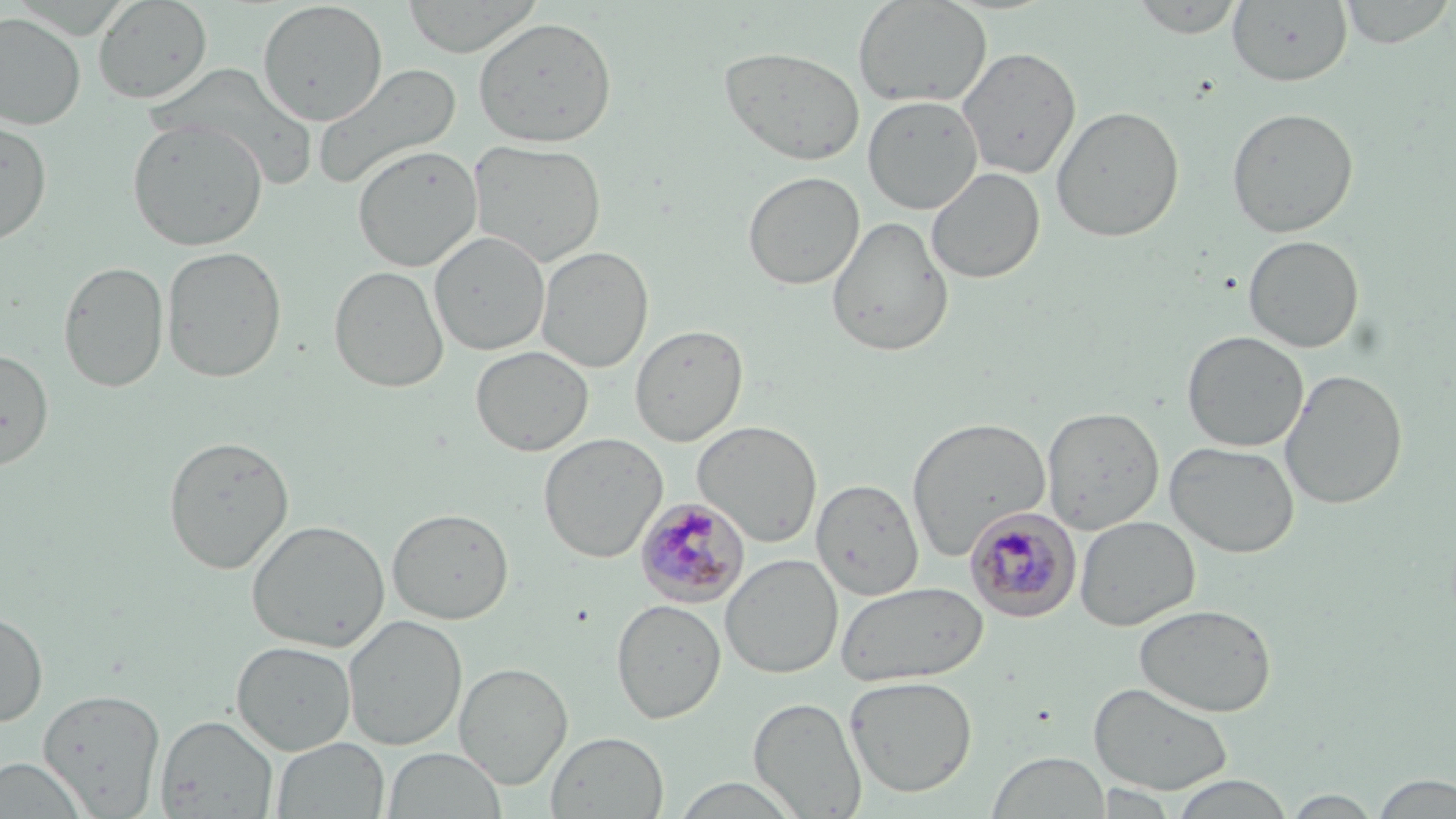
Summary:
  - Coordinate format: approximate bounding boxes as named x1/y1/x2/y2 corners in pixels
  - Plasmodium malariae-infected red blood cell locations: (x1=635, y1=497, x2=751, y2=606), (x1=965, y1=507, x2=1082, y2=622)
  - Uninfected red blood cell locations: (x1=92, y1=0, x2=213, y2=105), (x1=399, y1=0, x2=544, y2=58), (x1=853, y1=0, x2=992, y2=108), (x1=1129, y1=0, x2=1245, y2=38), (x1=1338, y1=0, x2=1455, y2=49), (x1=257, y1=1, x2=388, y2=126), (x1=1227, y1=1, x2=1353, y2=87), (x1=0, y1=12, x2=86, y2=130), (x1=472, y1=16, x2=617, y2=148), (x1=718, y1=45, x2=866, y2=166), (x1=956, y1=47, x2=1081, y2=179), (x1=312, y1=63, x2=462, y2=191), (x1=863, y1=95, x2=983, y2=214), (x1=1051, y1=105, x2=1185, y2=243), (x1=1226, y1=106, x2=1359, y2=238), (x1=0, y1=116, x2=52, y2=247), (x1=126, y1=118, x2=268, y2=252), (x1=469, y1=139, x2=608, y2=268), (x1=352, y1=144, x2=482, y2=272), (x1=926, y1=167, x2=1045, y2=284), (x1=742, y1=171, x2=865, y2=290), (x1=826, y1=215, x2=954, y2=357), (x1=429, y1=230, x2=550, y2=356), (x1=1243, y1=235, x2=1364, y2=353), (x1=535, y1=245, x2=654, y2=374), (x1=161, y1=246, x2=287, y2=383), (x1=58, y1=260, x2=169, y2=393), (x1=329, y1=265, x2=449, y2=393), (x1=630, y1=323, x2=748, y2=447), (x1=1182, y1=331, x2=1308, y2=452), (x1=470, y1=345, x2=594, y2=456), (x1=0, y1=348, x2=54, y2=471), (x1=1279, y1=369, x2=1408, y2=510), (x1=1042, y1=406, x2=1164, y2=533), (x1=906, y1=416, x2=1050, y2=561), (x1=693, y1=420, x2=822, y2=546), (x1=538, y1=433, x2=667, y2=563), (x1=163, y1=435, x2=294, y2=574), (x1=1164, y1=441, x2=1300, y2=558), (x1=811, y1=478, x2=924, y2=600), (x1=387, y1=507, x2=514, y2=624), (x1=1074, y1=515, x2=1200, y2=631), (x1=247, y1=519, x2=389, y2=653), (x1=720, y1=554, x2=843, y2=679), (x1=836, y1=581, x2=988, y2=687), (x1=611, y1=598, x2=726, y2=723), (x1=1133, y1=603, x2=1277, y2=717), (x1=0, y1=610, x2=48, y2=727), (x1=343, y1=614, x2=468, y2=750), (x1=231, y1=640, x2=357, y2=755), (x1=453, y1=662, x2=573, y2=789), (x1=844, y1=675, x2=978, y2=798), (x1=1088, y1=680, x2=1235, y2=795), (x1=38, y1=688, x2=166, y2=817), (x1=749, y1=696, x2=867, y2=818), (x1=156, y1=715, x2=279, y2=818), (x1=546, y1=731, x2=669, y2=818), (x1=271, y1=736, x2=390, y2=819), (x1=382, y1=747, x2=507, y2=819), (x1=987, y1=751, x2=1112, y2=819), (x1=0, y1=756, x2=89, y2=818), (x1=1371, y1=773, x2=1456, y2=818), (x1=1169, y1=774, x2=1294, y2=818), (x1=1092, y1=783, x2=1177, y2=816), (x1=1282, y1=790, x2=1383, y2=817)
  - Slide-level diagnosis: Plasmodium malariae
  - Magnification: 1000x
  - Preparation: thin blood smear
  - Field of view: single
  - Stain: May-Grünwald-Giemsa
  - Image size: 1456×819 pixels
  - Modality: light microscopy